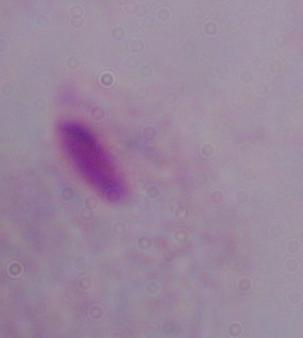

magnification = 1000x
identification = trichomonad
modality = photomicrograph